Find each parasitized red blood cell.
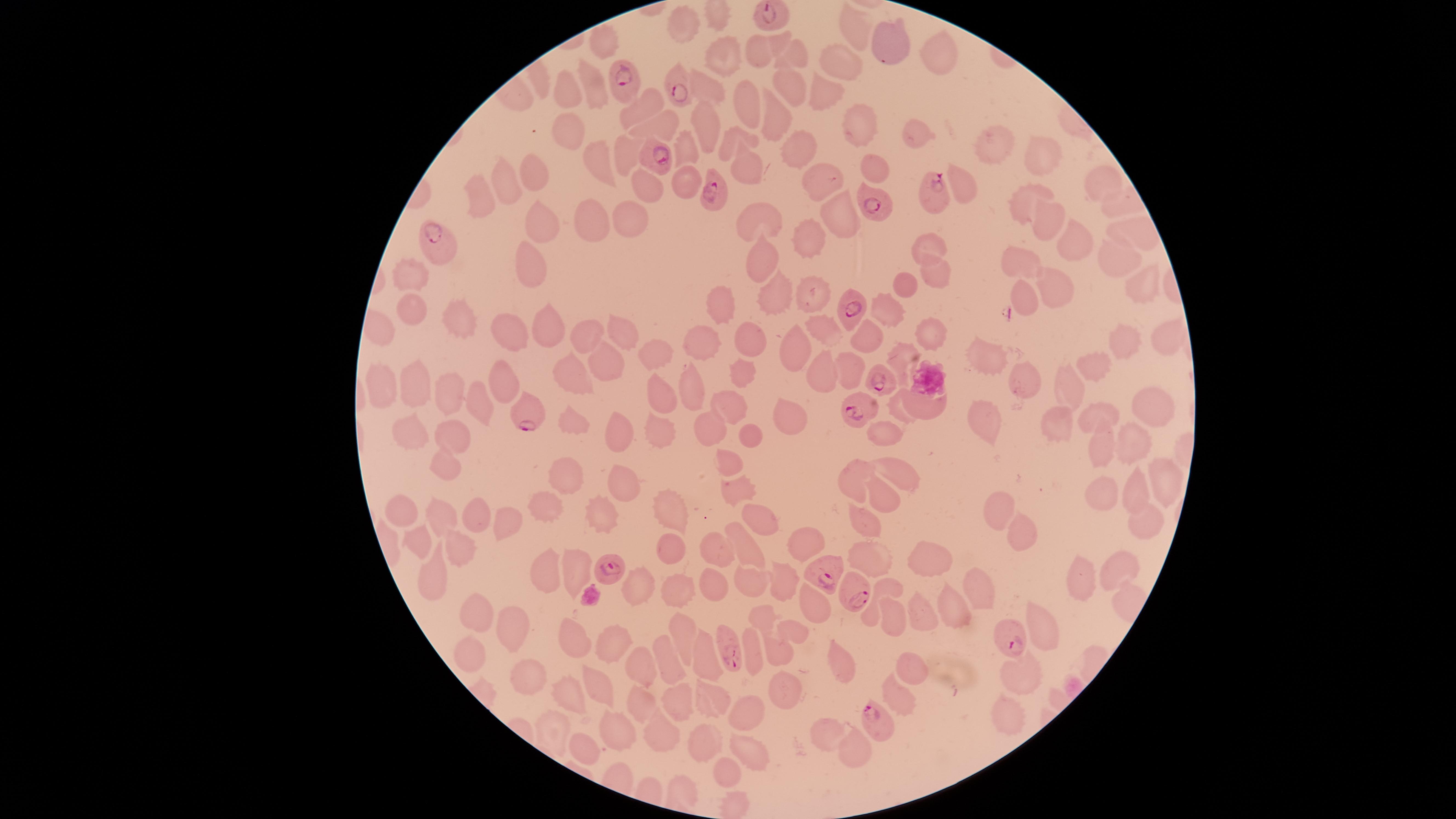
Approximate marker points, in pixels from the top-left corner.
Parasitized red blood cells: (x=768, y=17), (x=623, y=85), (x=675, y=86), (x=660, y=158), (x=717, y=198), (x=931, y=198), (x=872, y=201), (x=442, y=250), (x=853, y=308), (x=880, y=380), (x=862, y=407), (x=523, y=418), (x=609, y=570), (x=826, y=571), (x=856, y=593), (x=1011, y=634), (x=731, y=649), (x=874, y=721).

Approximate marker points, in pixels from the top-left corner. Uninfected red blood cells: (x=687, y=21), (x=859, y=27), (x=781, y=41), (x=888, y=42), (x=759, y=51), (x=944, y=52), (x=795, y=54), (x=724, y=56), (x=841, y=62), (x=788, y=83), (x=709, y=84), (x=594, y=87), (x=826, y=88), (x=570, y=90), (x=745, y=102), (x=645, y=105), (x=772, y=115), (x=566, y=122), (x=666, y=123), (x=705, y=123), (x=862, y=123), (x=917, y=134), (x=995, y=143), (x=686, y=144), (x=727, y=144), (x=627, y=148), (x=801, y=148), (x=1039, y=152), (x=596, y=161), (x=742, y=165), (x=875, y=169), (x=538, y=171), (x=823, y=178), (x=1102, y=180), (x=511, y=181), (x=688, y=181), (x=962, y=184), (x=1019, y=194), (x=482, y=195), (x=630, y=214), (x=840, y=215), (x=597, y=218), (x=759, y=220), (x=1048, y=220), (x=545, y=227), (x=1135, y=227), (x=814, y=238), (x=1076, y=241), (x=929, y=242), (x=761, y=255), (x=1022, y=255), (x=539, y=262), (x=1115, y=266), (x=933, y=269), (x=412, y=277), (x=908, y=283), (x=1137, y=285), (x=1056, y=288), (x=810, y=293), (x=1031, y=298), (x=779, y=299), (x=723, y=304), (x=411, y=308), (x=890, y=310), (x=456, y=315), (x=552, y=322), (x=827, y=328), (x=505, y=331), (x=591, y=334), (x=932, y=335), (x=624, y=336), (x=866, y=337), (x=756, y=339), (x=796, y=339), (x=1165, y=339), (x=707, y=343), (x=1122, y=343), (x=657, y=348), (x=902, y=351), (x=991, y=355), (x=607, y=360), (x=1096, y=363), (x=852, y=368), (x=744, y=370), (x=826, y=376), (x=1027, y=378), (x=694, y=380), (x=1068, y=380), (x=415, y=381), (x=503, y=381), (x=577, y=382), (x=383, y=383), (x=662, y=385), (x=448, y=391), (x=477, y=398), (x=1144, y=398), (x=731, y=406), (x=932, y=407), (x=896, y=408), (x=1105, y=418), (x=789, y=420), (x=990, y=420), (x=1066, y=422), (x=571, y=424), (x=410, y=428), (x=713, y=428), (x=661, y=430), (x=620, y=431), (x=890, y=431), (x=453, y=432), (x=753, y=434), (x=1132, y=440), (x=1101, y=448), (x=729, y=463), (x=449, y=465), (x=855, y=473), (x=900, y=473), (x=568, y=477), (x=1165, y=481), (x=618, y=483), (x=733, y=488), (x=1137, y=488), (x=1107, y=494), (x=887, y=497), (x=998, y=506), (x=547, y=508), (x=477, y=510), (x=403, y=511), (x=606, y=512), (x=762, y=512), (x=671, y=514), (x=447, y=515), (x=510, y=518), (x=867, y=518), (x=1147, y=523), (x=1018, y=531), (x=424, y=540), (x=804, y=544), (x=716, y=545), (x=461, y=549), (x=673, y=552), (x=872, y=552), (x=752, y=553), (x=940, y=558), (x=573, y=568), (x=1119, y=568), (x=547, y=569), (x=711, y=576), (x=1084, y=577), (x=444, y=578), (x=636, y=581), (x=782, y=583), (x=980, y=585), (x=676, y=586), (x=752, y=587), (x=894, y=593), (x=477, y=602), (x=954, y=603), (x=811, y=605), (x=929, y=613), (x=763, y=615), (x=894, y=620), (x=516, y=628), (x=797, y=631), (x=683, y=634), (x=1049, y=634), (x=575, y=640), (x=617, y=641), (x=469, y=647), (x=779, y=651), (x=754, y=656), (x=710, y=657), (x=670, y=660), (x=640, y=662), (x=843, y=665), (x=911, y=668), (x=1021, y=673), (x=537, y=674), (x=785, y=685), (x=599, y=686), (x=571, y=693), (x=900, y=694), (x=709, y=698), (x=641, y=701), (x=678, y=701), (x=749, y=708), (x=1009, y=713), (x=615, y=727), (x=661, y=732), (x=830, y=732), (x=550, y=733), (x=702, y=742), (x=586, y=747), (x=852, y=747), (x=749, y=748), (x=729, y=775). Image is 1456×819 pixels. Single field of view. Thin blood film. Smartphone photograph through the microscope eyepiece. Species: Plasmodium falciparum. Circular visible region. Giemsa-stained preparation.